Locate every Trypanosoma brucei.
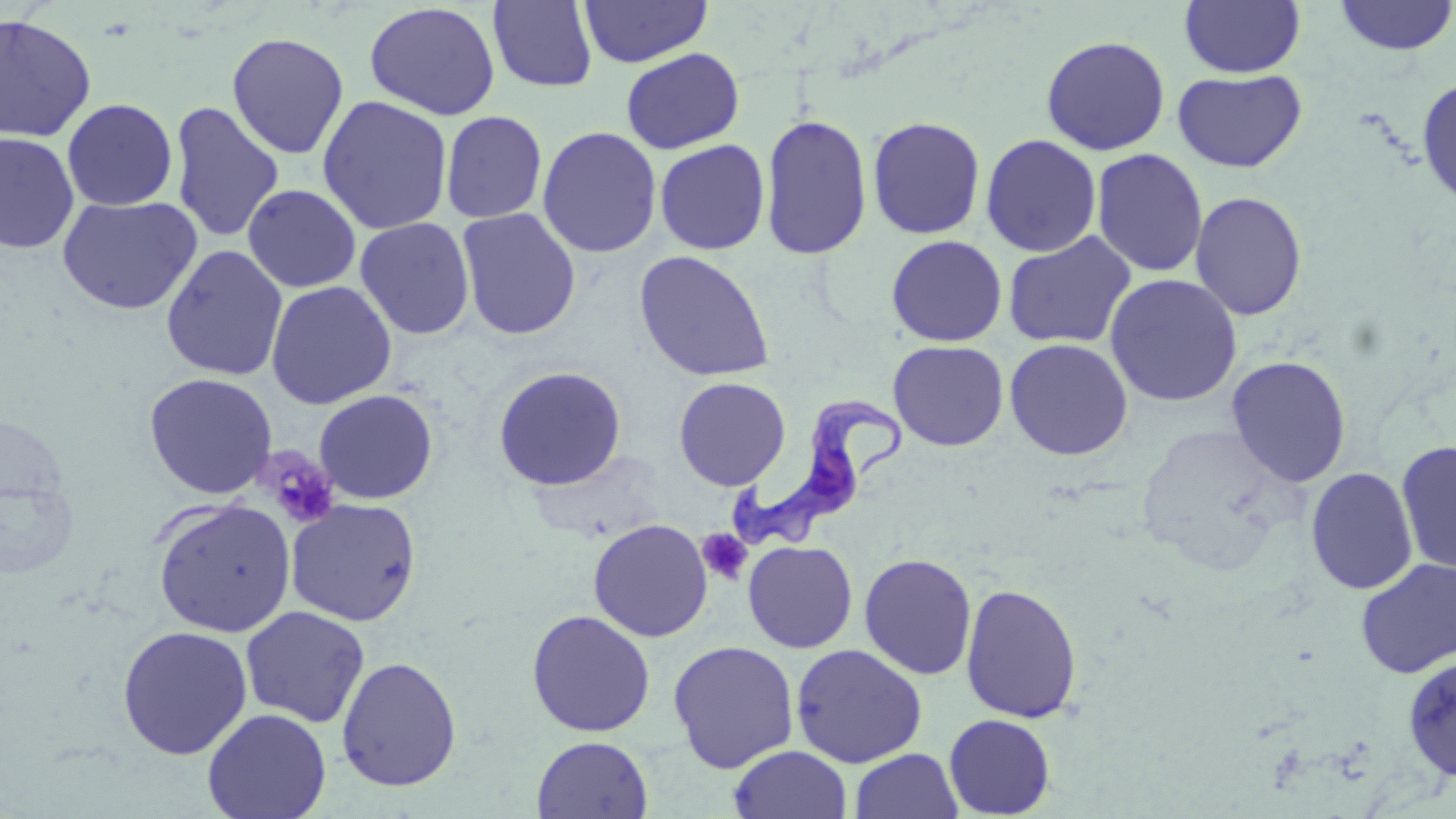
Approximate bounding boxes as (x1,y1)-(x2,y2) corner pairs in pixels.
Trypanosoma brucei: (729,392)-(906,556).

slide_level_diagnosis: Trypanosoma brucei
field_of_view: single
preparation: thin blood film
stain: May-Grünwald-Giemsa
uninfected_red_blood_cell_locations: 'approximate bounding boxes as (x1,y1)-(x2,y2) corner pairs in pixels: (580,0)-(712,68), (1179,0)-(1306,78), (1332,0)-(1455,56), (488,1)-(598,93), (364,2)-(501,120), (0,13)-(97,142), (227,33)-(349,158), (1040,35)-(1171,156), (621,47)-(744,154), (1173,69)-(1307,172), (1416,75)-(1456,209), (317,95)-(453,235), (62,98)-(178,211), (169,101)-(284,243), (441,111)-(547,224), (760,112)-(873,260), (867,116)-(986,239), (537,126)-(662,258), (0,133)-(79,254), (980,134)-(1102,257), (654,139)-(770,255), (1091,148)-(1209,278), (243,184)-(361,292), (1190,190)-(1308,321), (57,195)-(203,315), (456,208)-(582,341), (355,217)-(475,340), (1002,231)-(1137,349), (886,235)-(1007,347), (161,245)-(289,381), (634,251)-(776,382), (1104,273)-(1242,407), (265,280)-(397,409), (1004,338)-(1133,461), (888,340)-(1009,451), (1226,356)-(1351,488), (492,366)-(627,491), (143,372)-(278,500), (673,377)-(791,490), (314,389)-(438,504), (1396,439)-(1456,575), (1306,467)-(1418,595), (0,474)-(79,580), (285,498)-(422,627), (153,499)-(296,637), (588,518)-(713,642), (742,541)-(858,653), (859,553)-(977,680), (1355,558)-(1456,678), (960,583)-(1083,723), (240,606)-(370,728), (526,609)-(656,737), (117,625)-(253,760), (667,640)-(800,773), (790,643)-(928,768), (336,656)-(463,792), (1403,656)-(1456,781), (202,707)-(332,819), (944,713)-(1055,818), (531,736)-(653,819), (728,745)-(852,819), (849,748)-(963,819)'
modality: optical microscopy
image_size: 1456×819 pixels
platelet_locations: 'approximate bounding boxes as (x1,y1)-(x2,y2) corner pairs in pixels: (258,449)-(341,530), (697,527)-(754,586)'
magnification: 1000x